Report the malaria status of this cell.
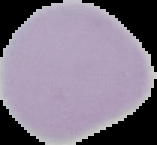
It is uninfected.

From a thin blood smear. Image is 157×145 pixels. Cell region segmented out of the field of view; the surrounding area is masked to black.